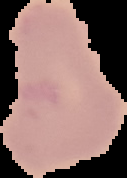
Summary:
  - Image type: cell region segmented out of the field of view; surrounding area masked to black
  - Preparation: thin blood smear
  - Image size: 127×178 pixels
  - Result: no Plasmodium parasites detected